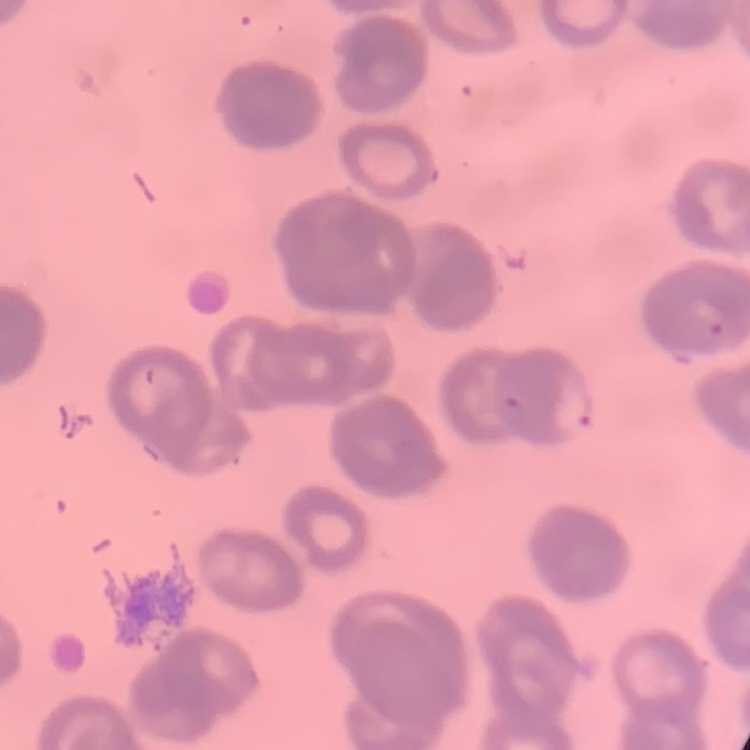

erythrocyte morphology = rouleaux formation
image type = square crop of a larger photomicrograph
stain = Field's or Giemsa
preparation = thin blood smear